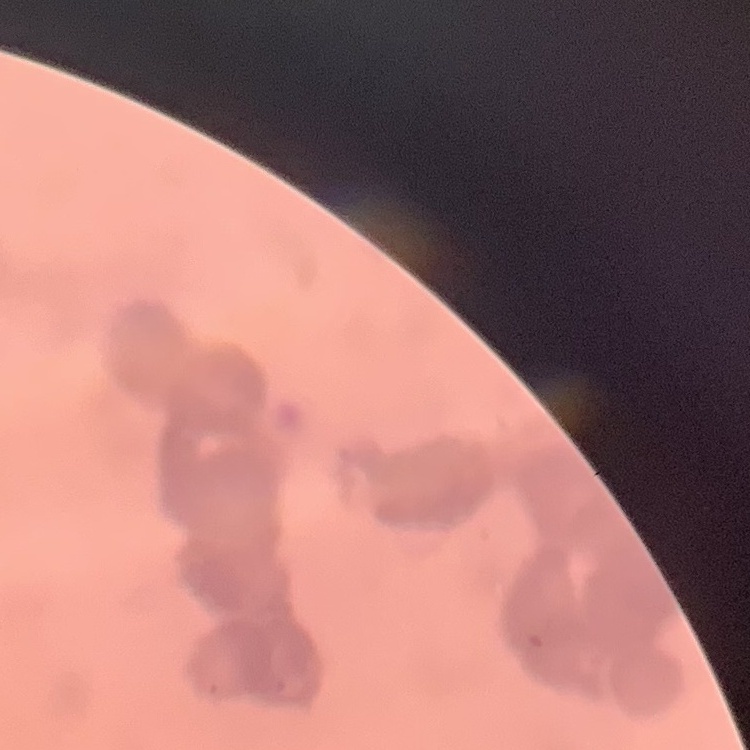

{
  "red_blood_cell_morphology": "rouleaux formation",
  "preparation": "thin blood smear",
  "image_type": "square crop of a larger photomicrograph",
  "stain": "Field's or Giemsa"
}